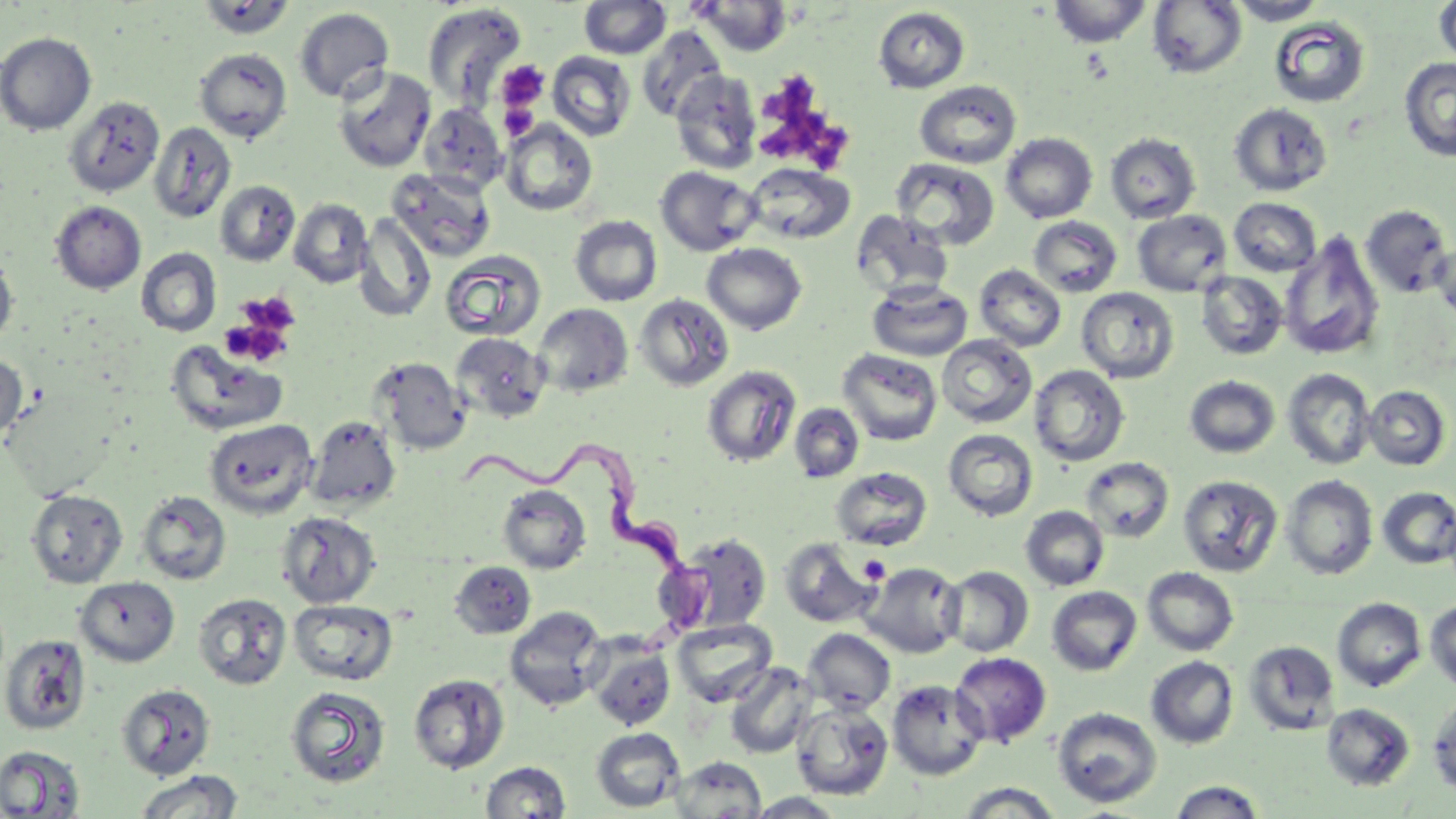 Approximate bounding boxes as (x1, y1, x2, y2) in pixels. Trypanosoma brucei locations: (446, 447, 715, 607). Uninfected red blood cell locations: (1048, 0, 1152, 47), (1226, 0, 1328, 25), (1434, 0, 1456, 67), (196, 1, 295, 40), (579, 1, 671, 59), (692, 1, 794, 57), (1148, 1, 1247, 78), (422, 2, 527, 109), (873, 6, 970, 93), (294, 8, 394, 103), (1269, 16, 1371, 108), (637, 27, 728, 122), (0, 32, 97, 135), (194, 48, 292, 143), (547, 51, 636, 141), (1399, 57, 1456, 161), (333, 66, 436, 172), (670, 70, 762, 175), (914, 80, 1022, 168), (64, 96, 164, 197), (419, 103, 507, 194), (1229, 103, 1332, 196), (500, 120, 598, 216), (149, 122, 236, 223), (1105, 132, 1201, 223), (1001, 133, 1098, 223), (891, 158, 999, 250), (744, 163, 854, 244), (655, 167, 760, 256), (386, 169, 496, 262), (215, 181, 300, 266), (1228, 197, 1321, 276), (289, 199, 372, 288), (51, 201, 146, 294), (1361, 205, 1453, 298), (851, 210, 954, 300), (1132, 210, 1231, 296), (354, 213, 436, 323), (569, 215, 662, 306), (1028, 216, 1123, 297), (1280, 232, 1385, 361), (1430, 239, 1456, 324), (702, 243, 807, 335), (0, 247, 18, 351), (136, 248, 221, 336), (440, 250, 546, 341), (974, 264, 1066, 351), (1196, 271, 1288, 360), (867, 281, 973, 362), (1076, 287, 1179, 383), (633, 293, 735, 392), (533, 303, 633, 397), (451, 333, 549, 423), (937, 334, 1037, 427), (164, 339, 290, 436), (838, 348, 943, 446), (0, 353, 27, 446), (370, 357, 470, 455), (702, 365, 801, 467), (1030, 365, 1130, 467), (1282, 368, 1377, 469), (1184, 375, 1280, 458), (1363, 386, 1451, 470), (789, 402, 864, 483), (307, 415, 401, 512), (204, 419, 317, 518), (943, 428, 1038, 521), (1081, 457, 1174, 542), (831, 467, 933, 550), (1178, 475, 1283, 577), (1281, 475, 1378, 580), (497, 485, 591, 574), (1377, 487, 1456, 569), (26, 489, 128, 589), (137, 490, 231, 585), (1020, 505, 1110, 591), (276, 511, 380, 609), (678, 533, 771, 632), (779, 537, 880, 628), (449, 561, 535, 639), (861, 561, 965, 657), (941, 565, 1034, 657), (1142, 566, 1239, 656), (75, 576, 180, 667), (1046, 586, 1142, 676), (192, 592, 292, 690), (1332, 597, 1426, 692), (288, 599, 398, 685), (1425, 599, 1456, 693), (504, 606, 609, 712), (672, 618, 777, 707), (802, 628, 896, 714), (1, 635, 90, 734), (1243, 639, 1341, 736), (587, 641, 677, 731), (951, 652, 1051, 748), (1146, 656, 1239, 749), (724, 662, 818, 759), (408, 673, 509, 774), (887, 678, 988, 780), (117, 683, 215, 780), (285, 685, 391, 788), (1427, 696, 1456, 795), (791, 701, 894, 800), (1321, 703, 1415, 790), (1052, 706, 1162, 808), (591, 727, 684, 812), (0, 745, 86, 818), (670, 756, 766, 817), (481, 761, 570, 818), (133, 770, 244, 818), (1168, 780, 1267, 818), (955, 783, 1066, 817), (745, 792, 847, 818). Platelet locations: (497, 60, 550, 114), (765, 73, 847, 167), (497, 102, 538, 137), (235, 292, 301, 338), (221, 305, 295, 365). Slide-level diagnosis: Trypanosoma brucei. May-Grünwald-Giemsa-stained preparation. Thin blood film. Single field of view. Image is 1456×819 pixels. Captured at 1000x magnification. Optical microscopy.